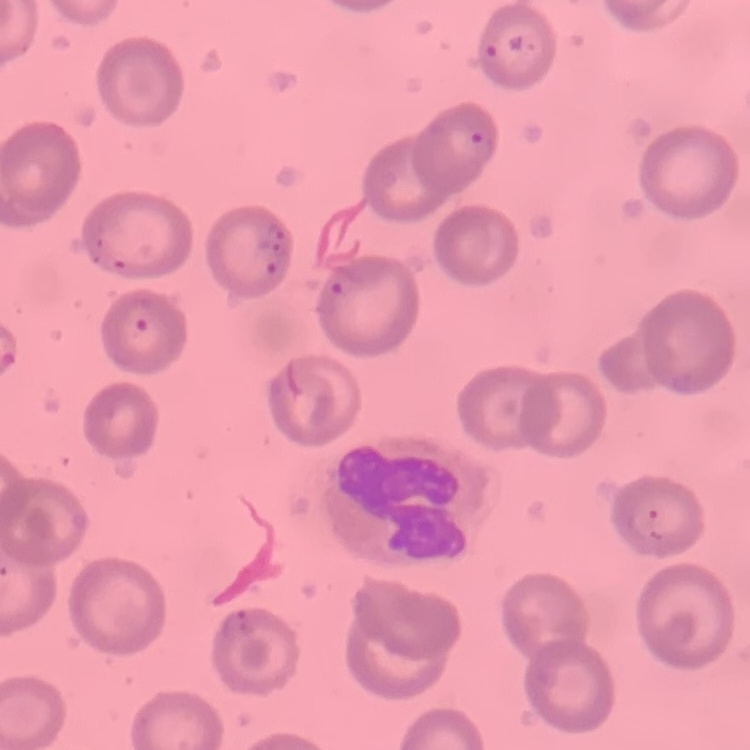
red blood cell morphology = no rouleaux formation
stain = Field's or Giemsa
preparation = thin peripheral smear
image type = square crop of a larger photomicrograph